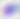
magnification = 400x
modality = micrograph
identification = Toxoplasma gondii